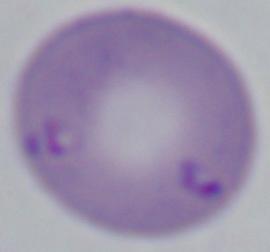
Summary:
  - Modality: micrograph
  - Identification: Babesia
  - Magnification: 1000x